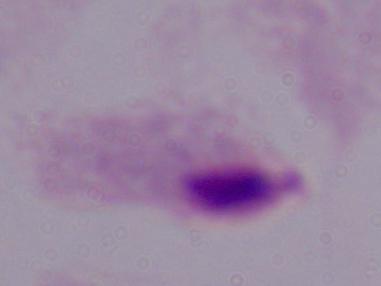

identification = trichomonad
modality = micrograph
magnification = 1000x